State which cell type is depicted.
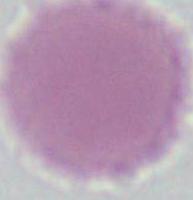
An erythrocyte.

magnification = 1000x
modality = photomicrograph